Locate every blood parasite and identify its species.
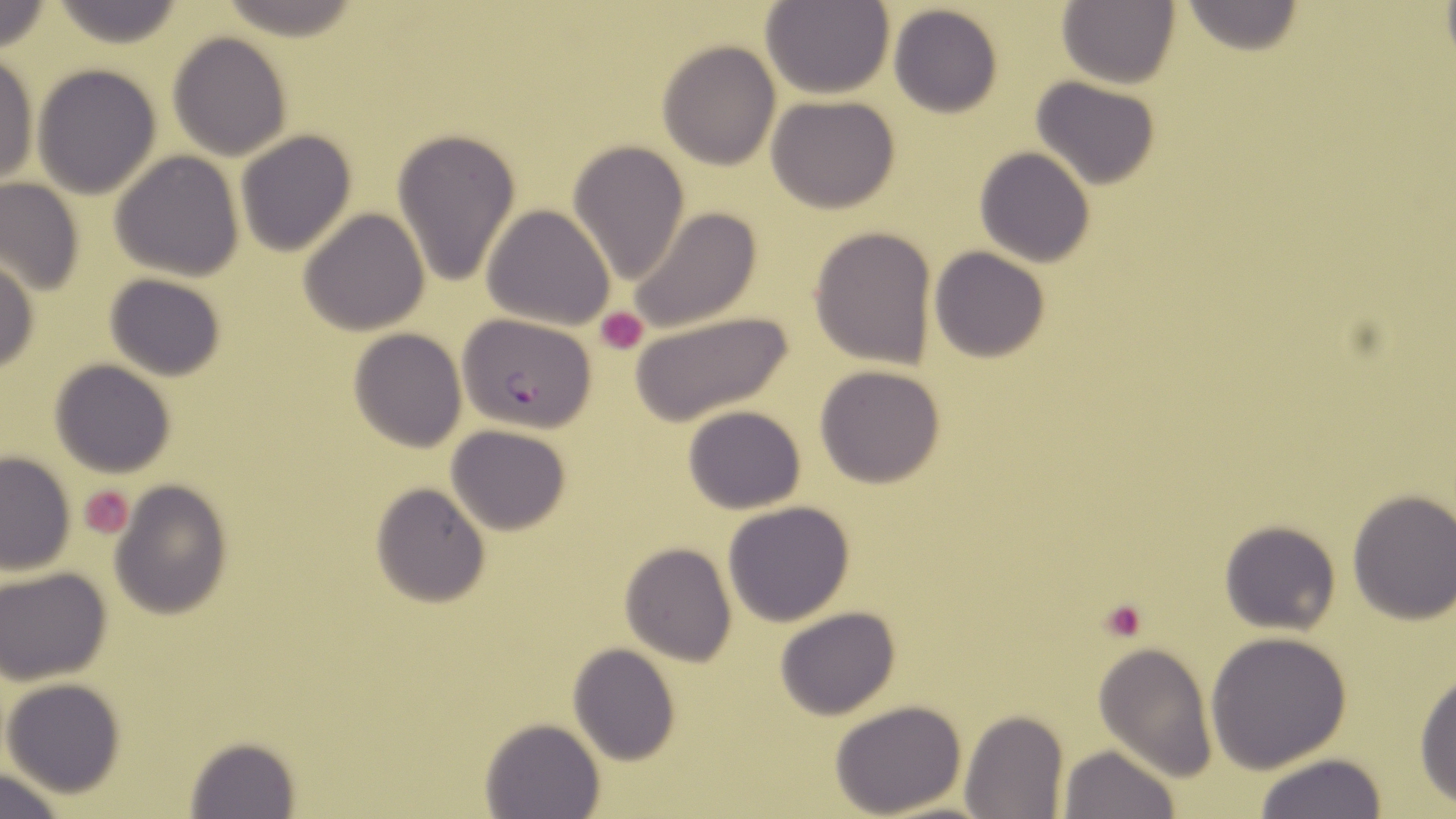
Approximate bounding boxes as [x1, y1, x2, y2] in pixels.
Plasmodium falciparum-infected red blood cells: [457, 312, 597, 433].
No Plasmodium ovale, Plasmodium malariae, Plasmodium vivax, Babesia divergens, or Trypanosoma brucei observed.

Platelet locations: [595, 307, 649, 355], [77, 485, 135, 539], [1099, 599, 1149, 645]. Uninfected red blood cell locations: [761, 0, 894, 99], [49, 1, 188, 49], [1057, 1, 1182, 90], [1177, 1, 1310, 56], [888, 4, 1004, 118], [166, 32, 293, 160], [658, 40, 781, 169], [0, 54, 38, 188], [31, 64, 162, 200], [1029, 76, 1162, 191], [766, 95, 902, 213], [235, 129, 357, 257], [393, 130, 522, 290], [567, 139, 690, 286], [974, 147, 1095, 269], [109, 150, 245, 281], [1, 179, 83, 296], [482, 204, 616, 330], [623, 206, 765, 335], [297, 209, 429, 336], [809, 226, 938, 369], [929, 247, 1052, 364], [0, 256, 38, 376], [104, 274, 229, 381], [623, 310, 797, 427], [347, 328, 467, 452], [49, 359, 177, 477], [813, 364, 948, 488], [682, 405, 807, 514], [445, 424, 573, 534], [0, 451, 77, 575], [110, 481, 234, 619], [370, 483, 491, 607], [1346, 490, 1456, 623], [723, 501, 854, 627], [1218, 524, 1341, 634], [620, 544, 737, 666], [1, 568, 113, 685], [773, 606, 901, 720], [1205, 631, 1355, 772], [568, 643, 681, 766], [1092, 644, 1217, 779], [1413, 669, 1456, 807], [2, 678, 126, 799], [828, 699, 968, 817], [962, 710, 1068, 819], [479, 717, 605, 819], [183, 736, 300, 817], [1057, 743, 1178, 819], [1251, 752, 1387, 818], [1, 770, 70, 818]. Slide-level diagnosis: Plasmodium falciparum. Captured at 1000x magnification. One field of a larger specimen. May-Grünwald-Giemsa-stained preparation. Light microscopy. Image is 1456×819 pixels. Thin blood smear.